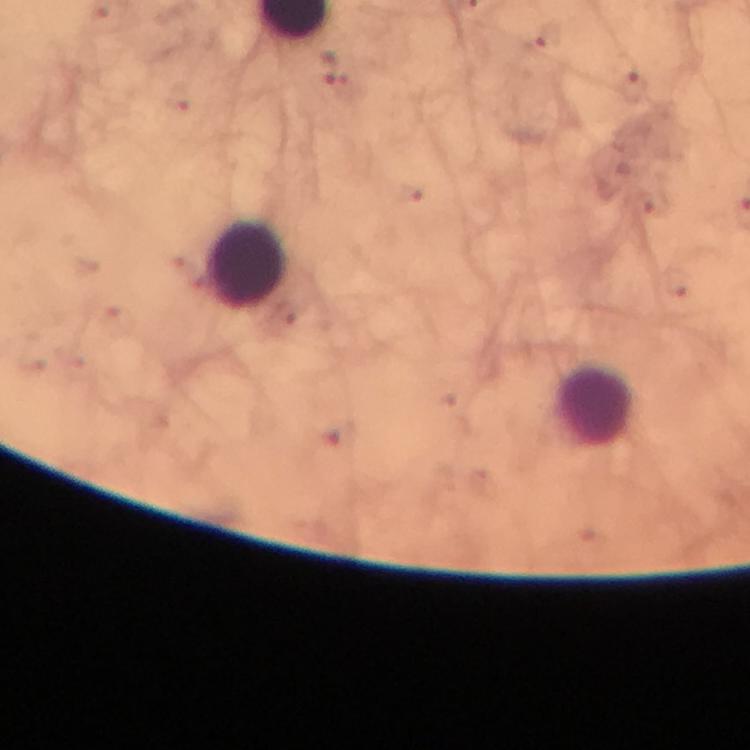

{
  "cropped_from": "a single field of view",
  "plasmodium_parasite_locations": "approximate centers as {x, y} in pixels: {550, 36}, {629, 88}, {344, 89}",
  "image_size": "750×750 pixels",
  "immersion_oil": "applied",
  "leukocyte_locations": "approximate centers as {x, y} in pixels: {247, 265}, {593, 404}",
  "magnification": "100x",
  "stain": "Giemsa",
  "context": "from a malaria diagnostic workup",
  "capture": "smartphone photograph through a microscope",
  "preparation": "thick blood film"
}